Point out malaria parasites and leukocytes.
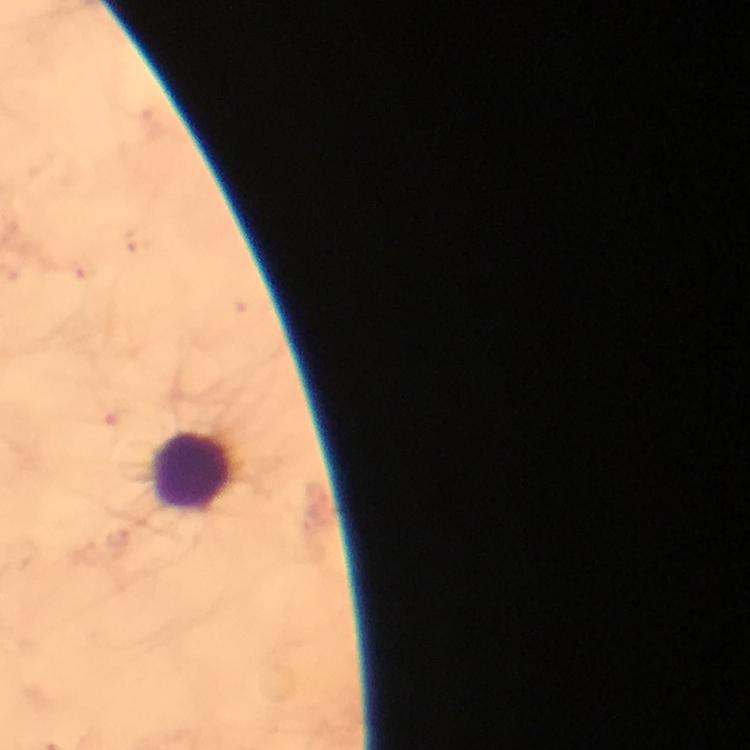
No malaria parasites seen.
Approximate centers as (x, y) in pixels.
Leukocytes: (194, 473).

Summary:
  - Stain: Giemsa
  - Preparation: thick blood smear
  - Image size: 750×750 pixels
  - Magnification: 100x
  - Cropped from: a single field of view
  - Immersion oil: applied
  - Capture: smartphone mounted on the microscope
  - Context: from a diagnostic examination for malaria